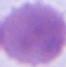
identification: erythrocyte
modality: photomicrograph
magnification: 1000x